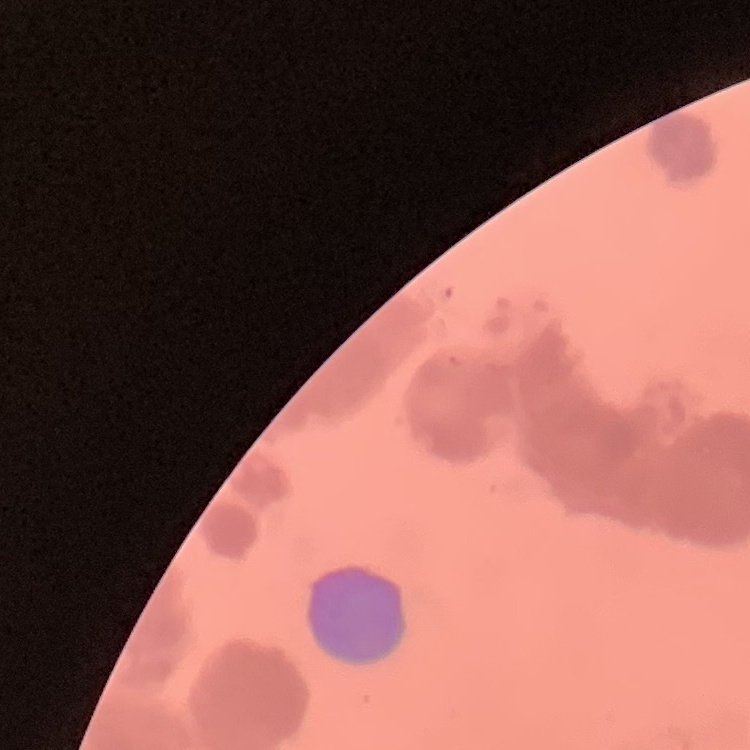

The red blood cells show rouleaux formation. One tile cut from a larger photomicrograph. Field's or Giemsa stain. Thin blood smear.